State which parasite is depicted.
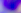
This is Toxoplasma gondii.

Summary:
  - Modality: micrograph
  - Magnification: 400x